Report the malaria status of this cell.
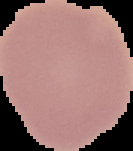

It is uninfected.

Summary:
  - Image size: 133×151 pixels
  - Image type: segmented cell region on a black background
  - Preparation: thin blood film